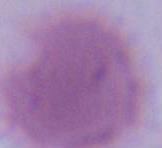
Photomicrograph. Captured at 1000x magnification. A red blood cell is seen.